Identify the parasite.
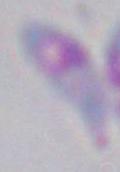
Toxoplasma gondii.

Photomicrograph. Captured at 1000x magnification.